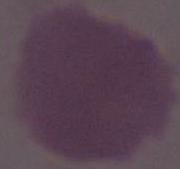

{
  "modality": "photomicrograph",
  "identification": "red blood cell",
  "magnification": "1000x"
}